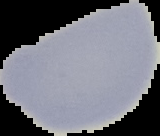
result = negative for malaria parasites
preparation = thin blood smear
image type = cell region segmented out of the field of view; surrounding area masked to black
image size = 160×136 pixels